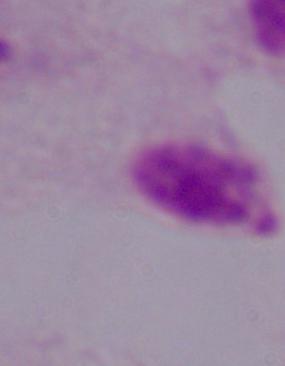
identification = trichomonad
magnification = 1000x
modality = photomicrograph